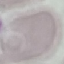

result: no malaria parasites seen
preparation: thin smear
capture: smartphone camera at the microscope eyepiece
stain: Giemsa
image_type: automatically extracted cell patch, resized to 64 × 64 pixels